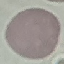
Malaria status: uninfected. Acquired by smartphone through the microscope eyepiece. Thin blood film. Automatically extracted cell patch, resized to 64 × 64 pixels. Giemsa stain.